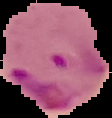

preparation: thin blood film
malaria_status: parasitized
image_type: segmented cell region on a black background
image_size: 112×118 pixels